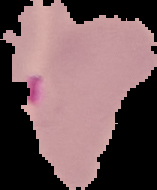

Summary:
  - Malaria status: parasitized
  - Preparation: thin blood film
  - Image size: 157×190 pixels
  - Image type: segmented cell region with the area outside set to black